Classify this cell by malaria status.
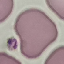
It is uninfected.

Giemsa stain. Automatically extracted cell patch, resized to 64 × 64 pixels. Photographed with a smartphone camera at the microscope eyepiece. Thin blood film.